Comment on the morphology of the erythrocytes.
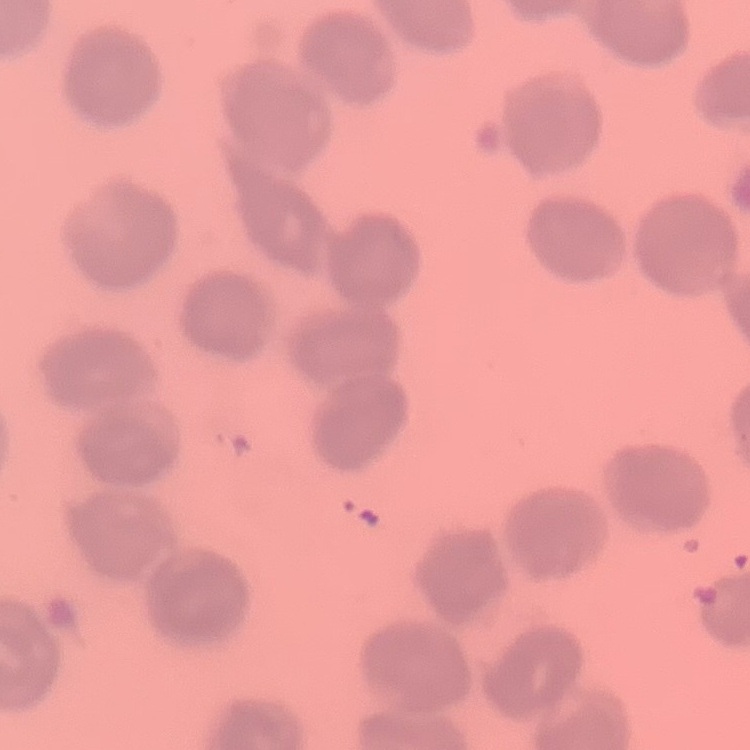

No rouleaux formation.

Stained with either Field's or Giemsa. Thin blood smear. One tile cut from a larger photomicrograph.